Assess this cell for malaria.
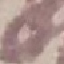

Uninfected.

stain = Giemsa
preparation = thin smear
image type = cell patch, automatically extracted from a larger field of view and resized to 64 × 64 pixels
capture = smartphone camera at the microscope eyepiece